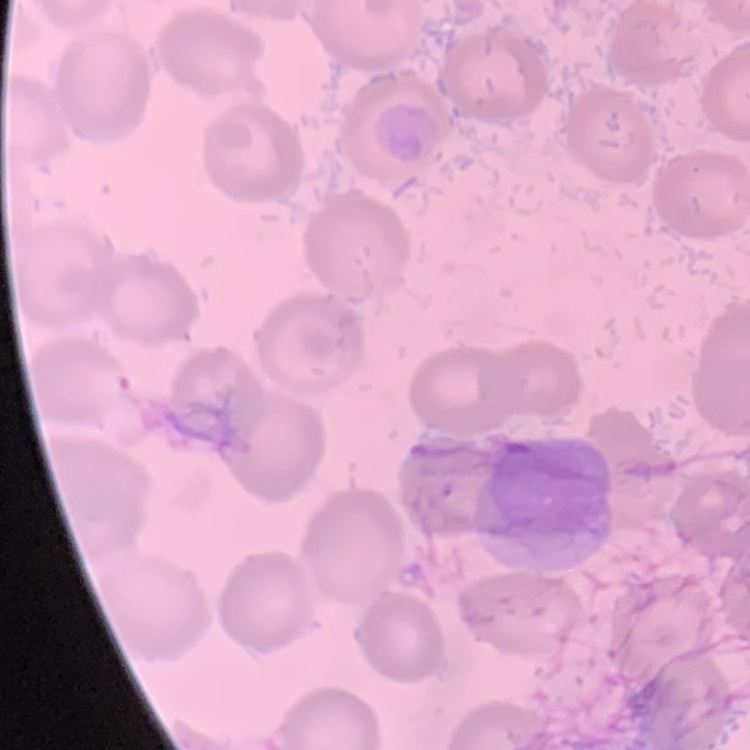 The erythrocytes show no rouleaux formation. Thin blood smear. One tile cut from a larger photomicrograph. Field's or Giemsa stain.